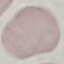 Result: no malaria parasites detected. Thin blood smear. Giemsa-stained preparation. Photographed with a smartphone camera at the microscope eyepiece. Cell patch, automatically extracted from a larger field of view and resized to 64 × 64 pixels.